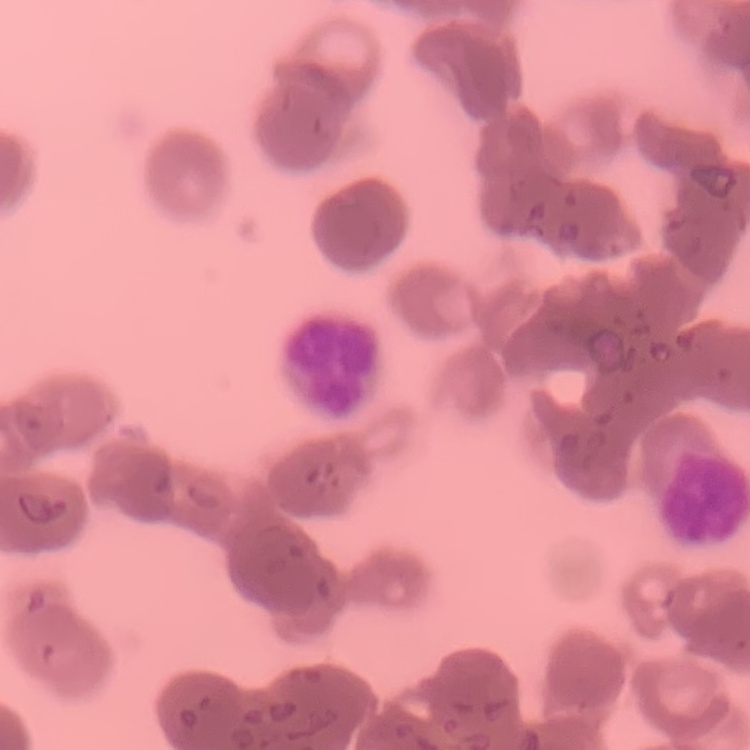
Summary:
  - Red blood cell morphology: rouleaux formation
  - Preparation: thin peripheral smear
  - Stain: Field's or Giemsa
  - Image type: one tile cut from a larger photomicrograph